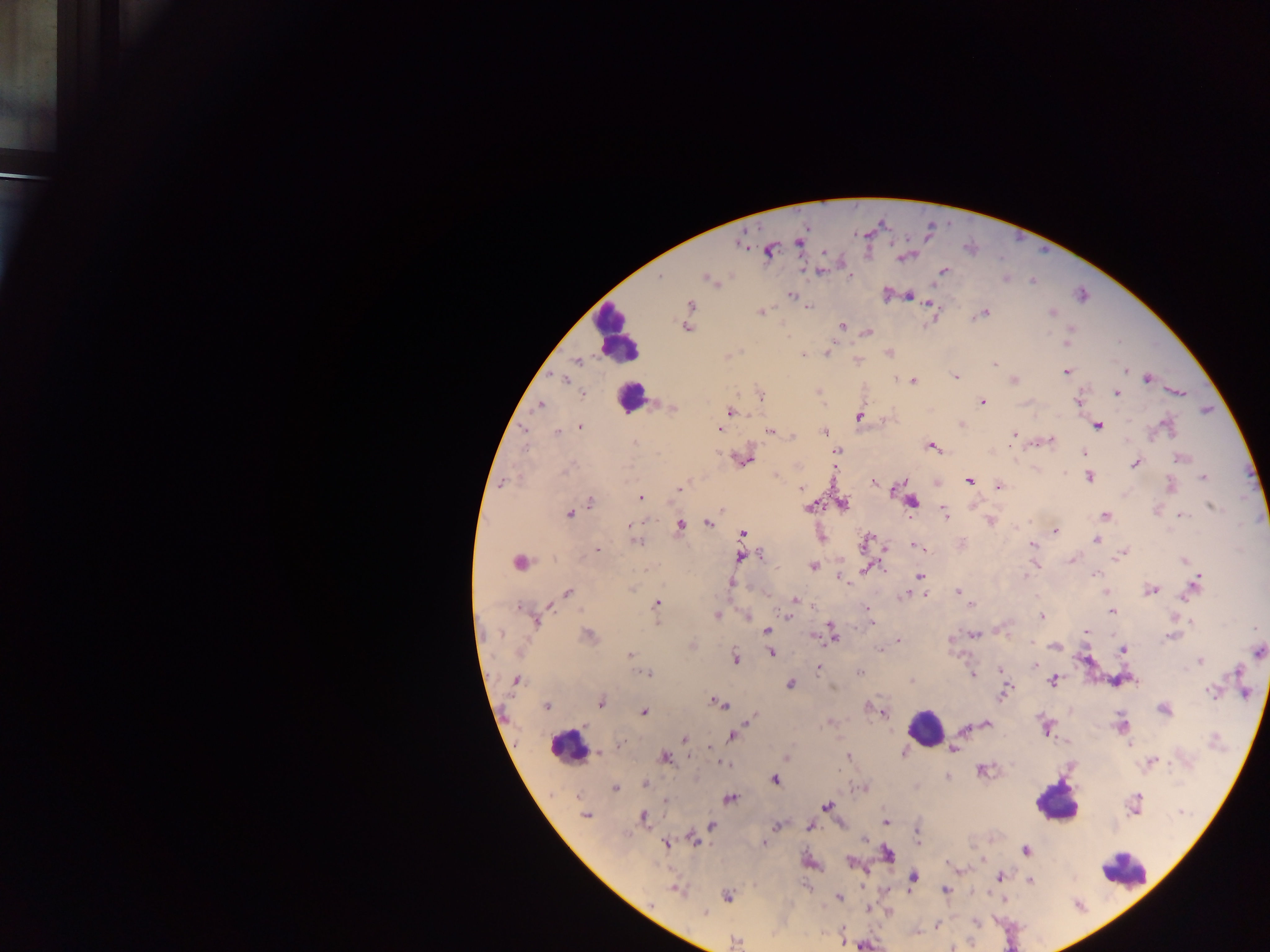

image size = 1270×952 pixels
country = Ghana
preparation = thick blood smear
Plasmodium parasite locations = approximate centers as (x, y) in pixels: (799, 241), (741, 243), (769, 251), (903, 257), (844, 268), (848, 270), (821, 271), (943, 271), (660, 277), (1005, 278), (709, 280), (887, 293), (792, 295), (906, 295), (930, 304), (689, 305), (807, 306), (760, 312), (1051, 312), (983, 313), (686, 326), (842, 327), (1069, 331), (867, 332), (1065, 344), (827, 352), (888, 353), (804, 354), (727, 357), (857, 360), (575, 361), (995, 363), (1125, 369), (1067, 371), (954, 375), (563, 378), (1146, 378), (912, 380), (1013, 380), (818, 392), (1115, 392), (1177, 392), (581, 393), (759, 394), (1077, 401), (982, 402), (540, 405), (671, 408), (729, 412), (861, 416), (961, 423), (1097, 425), (1167, 426), (580, 427), (718, 427), (524, 430), (769, 430), (557, 432), (823, 432), (1014, 433), (790, 436), (1051, 440), (633, 442), (932, 446), (837, 450), (1084, 453), (1180, 458), (743, 459), (1136, 462), (1089, 476), (1203, 477), (969, 480), (501, 482), (874, 483), (937, 483), (999, 486), (1170, 486), (678, 487), (800, 488), (640, 497), (590, 501), (910, 502), (841, 504), (811, 506), (1211, 506), (1156, 510), (569, 513), (943, 513), (1179, 515), (1105, 516), (989, 520), (708, 523), (630, 525), (681, 526), (1054, 531), (742, 534), (821, 534), (1096, 540), (634, 541), (867, 542), (962, 543), (915, 545), (1032, 545), (596, 550), (1120, 554), (740, 556), (1072, 559), (1185, 560), (519, 561), (1035, 563), (812, 566), (865, 570), (839, 576), (919, 576), (731, 582), (1195, 584), (1151, 589), (957, 591), (1107, 592), (568, 593), (925, 594), (904, 595), (794, 600), (656, 603), (972, 605), (549, 606), (867, 607), (1112, 612), (716, 615), (747, 615), (788, 616), (1041, 616), (534, 620), (1190, 622), (870, 623), (766, 631), (1084, 631), (972, 634), (832, 635), (588, 636), (1173, 636), (949, 639), (898, 640), (692, 645), (1054, 645), (879, 649), (1122, 650), (771, 652), (1259, 652), (630, 655), (735, 658), (1200, 661), (1035, 664), (818, 668), (1000, 670), (858, 672), (648, 673), (971, 674), (911, 680), (1052, 680), (515, 681), (1117, 681), (790, 684), (1212, 692), (1003, 693), (600, 701), (716, 702), (547, 706), (867, 708), (1163, 709), (643, 712), (883, 713), (748, 720), (829, 721), (984, 723), (1122, 725), (1046, 727), (967, 728), (732, 735), (684, 739), (1065, 742), (620, 744), (1130, 744), (710, 747), (953, 748), (600, 751), (847, 756), (663, 757), (785, 757), (721, 762), (1151, 762), (981, 769), (947, 776), (775, 779), (645, 784), (862, 787), (614, 788), (729, 798), (666, 801), (1134, 805), (826, 807), (585, 815), (644, 817), (884, 820), (711, 825), (777, 825), (810, 825), (917, 832), (693, 838), (917, 839), (665, 843), (764, 843), (1025, 850), (886, 853), (809, 862), (850, 862), (954, 869), (958, 870), (912, 876), (999, 877), (1028, 879), (676, 889), (945, 889), (727, 896), (839, 897), (868, 908), (888, 910), (704, 914), (975, 923), (937, 924), (915, 932), (735, 942)
leukocyte locations = approximate centers as (x, y) in pixels: (617, 334), (630, 396), (925, 727), (567, 747), (1057, 801), (1123, 871)
capture = mobile-phone photograph through a microscope
field of view = single